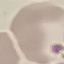

result: no malaria parasites seen
stain: Giemsa
image_type: automatically extracted cell patch, resized to 64 × 64 pixels
capture: smartphone camera at the microscope eyepiece
preparation: thin blood smear